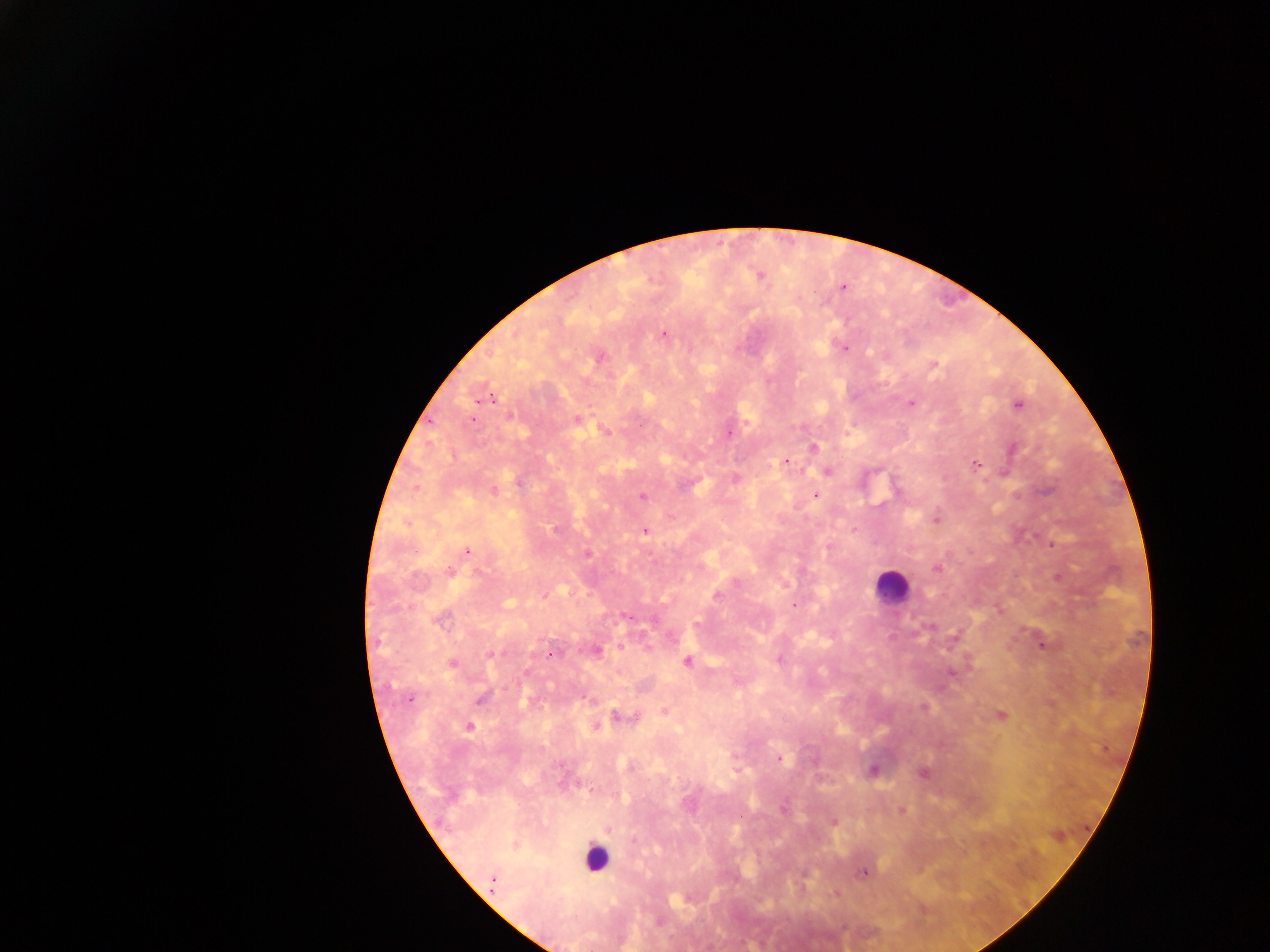
Approximate centers as x y in pixels.
Summary:
  - Malaria parasite locations: 759 276; 842 287; 663 334; 843 348; 599 358; 934 365; 486 398; 912 403; 1017 405; 472 419; 577 419; 606 430; 728 433; 814 447; 1013 449; 786 461; 976 465; 827 471; 1005 472; 736 478; 518 482; 493 490; 815 496; 642 497; 936 520; 854 529; 556 531; 645 531; 829 547; 467 551; 587 554; 937 569; 449 572; 480 573; 717 596; 794 605; 627 616; 440 620; 931 627; 1043 644; 620 646; 595 650; 491 655; 552 655; 779 660; 687 661; 452 664; 951 674; 481 698; 410 699; 924 707; 664 710; 1001 715; 620 716; 470 727; 597 727; 779 758; 873 770; 923 772; 784 809; 902 810; 607 830; 514 845; 863 873; 493 884
  - Leukocyte locations: 891 586; 596 859
  - Country: Ghana
  - Field of view: single
  - Capture: mobile-phone photograph through a microscope
  - Image size: 1270×952 pixels
  - Preparation: thick blood film